State which cell type is depicted.
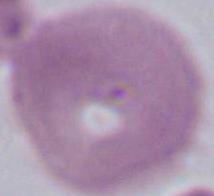

This is an erythrocyte.

Summary:
  - Magnification: 1000x
  - Modality: micrograph